Identify the cell.
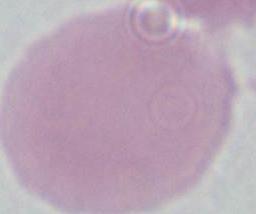

An erythrocyte.

Summary:
  - Modality: photomicrograph
  - Magnification: 1000x